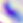
Summary:
  - Identification: Toxoplasma gondii
  - Modality: micrograph
  - Magnification: 400x